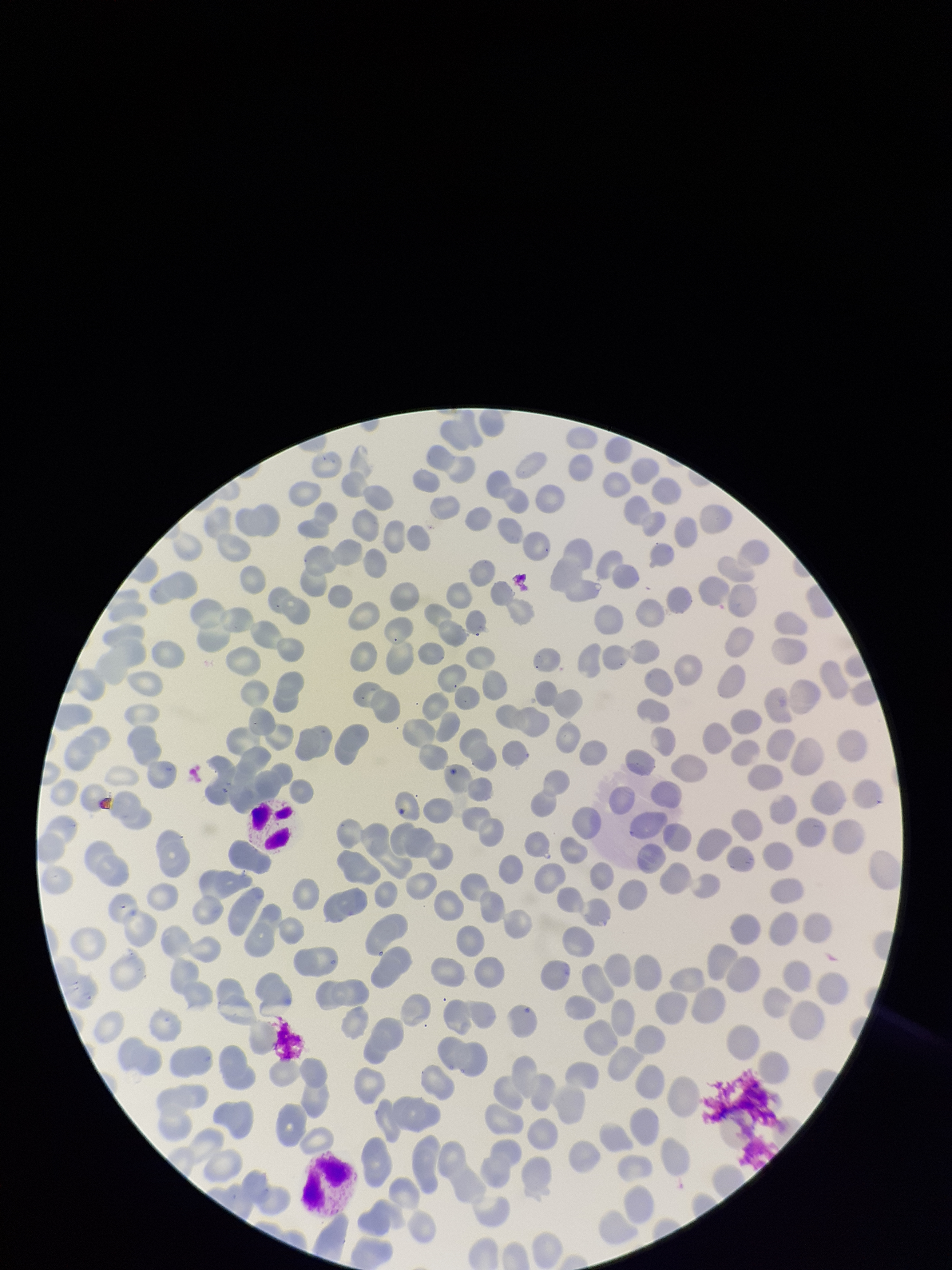
Summary:
  - Preparation: thin
  - Parasitized red blood cells: none identified
  - Image size: 952×1270 pixels
  - Stain: Giemsa
  - Field of view: single
  - Capture: smartphone photograph through the microscope eyepiece
  - Red blood cell count: 238
  - Parasitized red blood cell count: 0
  - Patient malaria status: negative